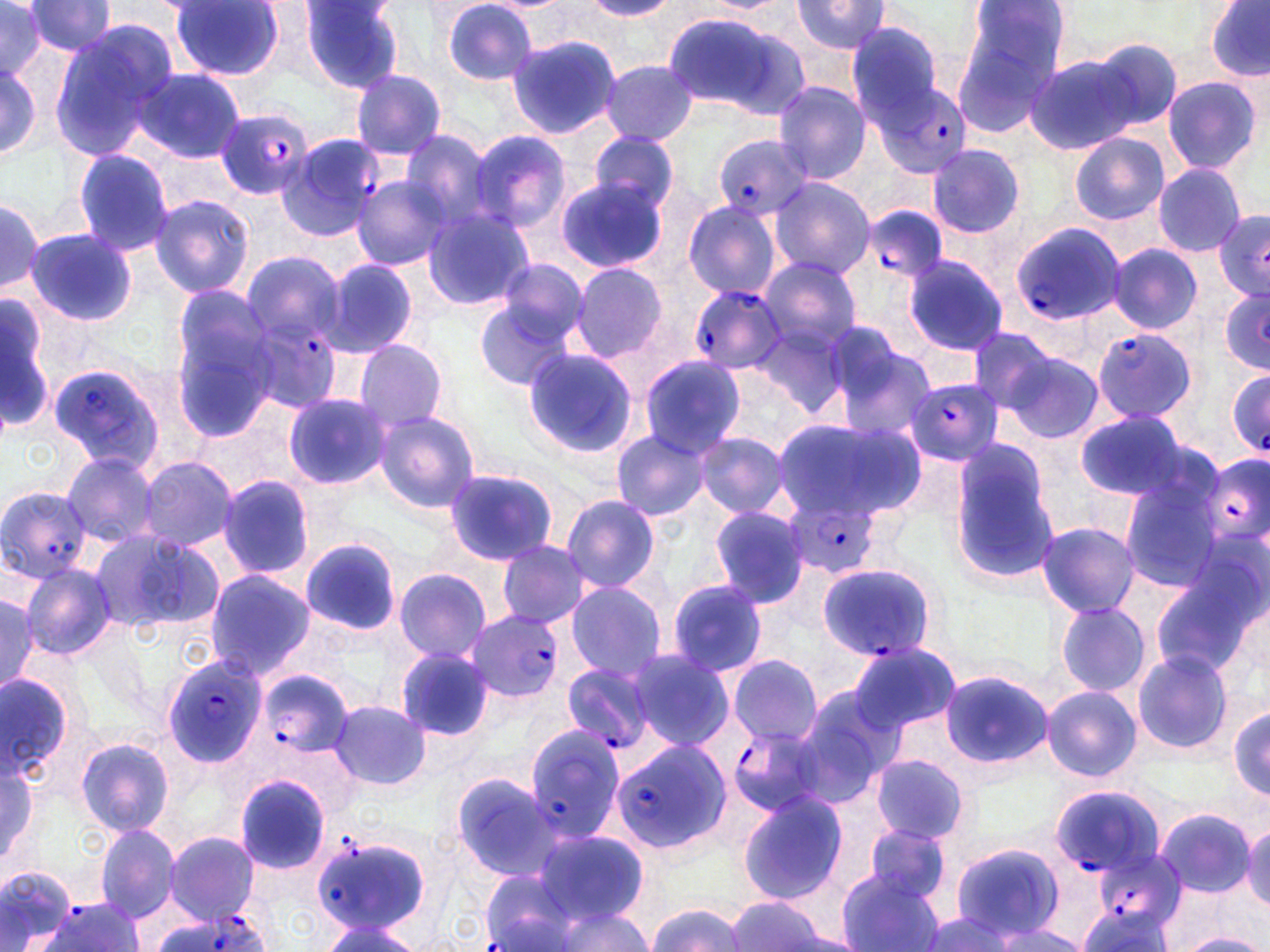
Approximate bounding boxes as (x1, y1, x2, y2) in pixels. Uninfected red blood cell locations (subset): (581, 0, 680, 20), (702, 0, 795, 13), (949, 0, 1072, 129), (1205, 0, 1270, 82), (24, 1, 118, 56), (299, 1, 409, 94), (441, 1, 540, 84), (788, 1, 894, 57), (170, 2, 287, 80), (0, 3, 56, 82), (659, 10, 807, 118), (844, 20, 948, 123), (51, 22, 179, 154), (505, 34, 622, 141), (1083, 37, 1184, 134), (0, 53, 43, 165), (1026, 53, 1146, 154), (600, 60, 699, 144), (135, 67, 244, 164), (351, 70, 447, 159), (1161, 76, 1262, 175), (772, 82, 872, 182), (399, 128, 501, 232), (467, 129, 571, 233), (588, 132, 680, 216), (1069, 132, 1170, 227), (926, 144, 1025, 239), (70, 147, 175, 256), (1151, 163, 1247, 258), (351, 176, 452, 271), (767, 177, 876, 279), (556, 181, 667, 273), (0, 193, 44, 300), (150, 194, 255, 298), (681, 200, 783, 300), (422, 209, 536, 311), (24, 227, 137, 327), (1108, 244, 1203, 335), (241, 250, 346, 349), (758, 255, 863, 353), (902, 255, 1009, 355), (320, 259, 419, 359), (491, 259, 591, 348), (569, 262, 668, 363), (0, 296, 54, 437), (167, 296, 279, 435), (473, 300, 577, 389), (751, 314, 851, 419), (966, 326, 1059, 415), (827, 333, 935, 442), (353, 340, 449, 433), (521, 348, 639, 457), (999, 349, 1105, 446), (638, 355, 744, 455), (303, 357, 444, 473), (283, 393, 388, 489), (1075, 408, 1191, 503), (373, 410, 481, 514), (771, 416, 917, 523), (611, 431, 709, 521), (693, 432, 791, 518), (945, 442, 1062, 584), (60, 451, 160, 549), (134, 455, 239, 551), (444, 468, 559, 565), (217, 475, 316, 580), (1117, 478, 1221, 593), (560, 494, 661, 593), (708, 505, 811, 609), (1035, 521, 1140, 616), (89, 528, 223, 637), (300, 538, 402, 637), (496, 540, 590, 629), (1148, 561, 1265, 684), (19, 564, 117, 661), (394, 568, 492, 663), (203, 569, 317, 678), (563, 580, 669, 679), (665, 580, 767, 677), (0, 592, 41, 699), (1055, 600, 1152, 697), (845, 641, 959, 736), (396, 647, 498, 740), (626, 650, 733, 750), (1132, 650, 1232, 756), (727, 655, 822, 745), (938, 668, 1053, 769), (0, 671, 75, 781), (790, 685, 899, 805), (1039, 686, 1142, 782), (330, 700, 432, 791), (1230, 704, 1269, 797), (74, 735, 174, 835), (869, 756, 970, 845), (0, 757, 38, 867), (449, 773, 562, 880), (737, 791, 850, 904), (1152, 806, 1259, 898), (1241, 819, 1270, 911), (93, 823, 182, 924), (862, 823, 957, 905), (531, 829, 649, 927), (163, 832, 261, 922), (950, 843, 1064, 942), (0, 865, 77, 949), (836, 870, 943, 952), (724, 897, 833, 952), (646, 901, 745, 952), (543, 906, 659, 951), (912, 913, 1017, 951), (316, 918, 425, 952), (986, 921, 1091, 952), (1176, 933, 1267, 952). Plasmodium falciparum-infected red blood cell locations (subset): (874, 82, 972, 178), (214, 106, 315, 200), (276, 131, 384, 242), (713, 134, 815, 222), (869, 207, 946, 284), (1010, 224, 1126, 329), (686, 285, 785, 374), (242, 316, 342, 416), (1090, 330, 1197, 423), (47, 360, 165, 470), (1226, 367, 1270, 459), (902, 378, 1004, 467), (1196, 453, 1268, 561), (0, 485, 94, 583), (782, 489, 885, 579), (817, 562, 937, 659), (467, 610, 565, 703), (160, 655, 267, 769), (559, 661, 659, 756), (254, 666, 354, 767), (523, 724, 633, 841), (728, 726, 830, 817), (610, 740, 729, 853), (1048, 785, 1163, 884), (311, 833, 431, 937), (1094, 849, 1184, 934), (478, 871, 583, 952), (39, 899, 144, 951), (148, 910, 271, 952). Slide-level diagnosis: Plasmodium falciparum. Image is 1270×952 pixels. Optical microscopy. 1000x magnification. One field of a larger specimen. Thin blood smear. May-Grünwald-Giemsa-stained preparation.